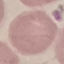
{
  "result": "no malaria parasites seen",
  "preparation": "thin blood smear",
  "image_type": "automatically extracted cell patch, resized to 64 × 64 pixels",
  "stain": "Giemsa",
  "capture": "smartphone camera at the microscope eyepiece"
}